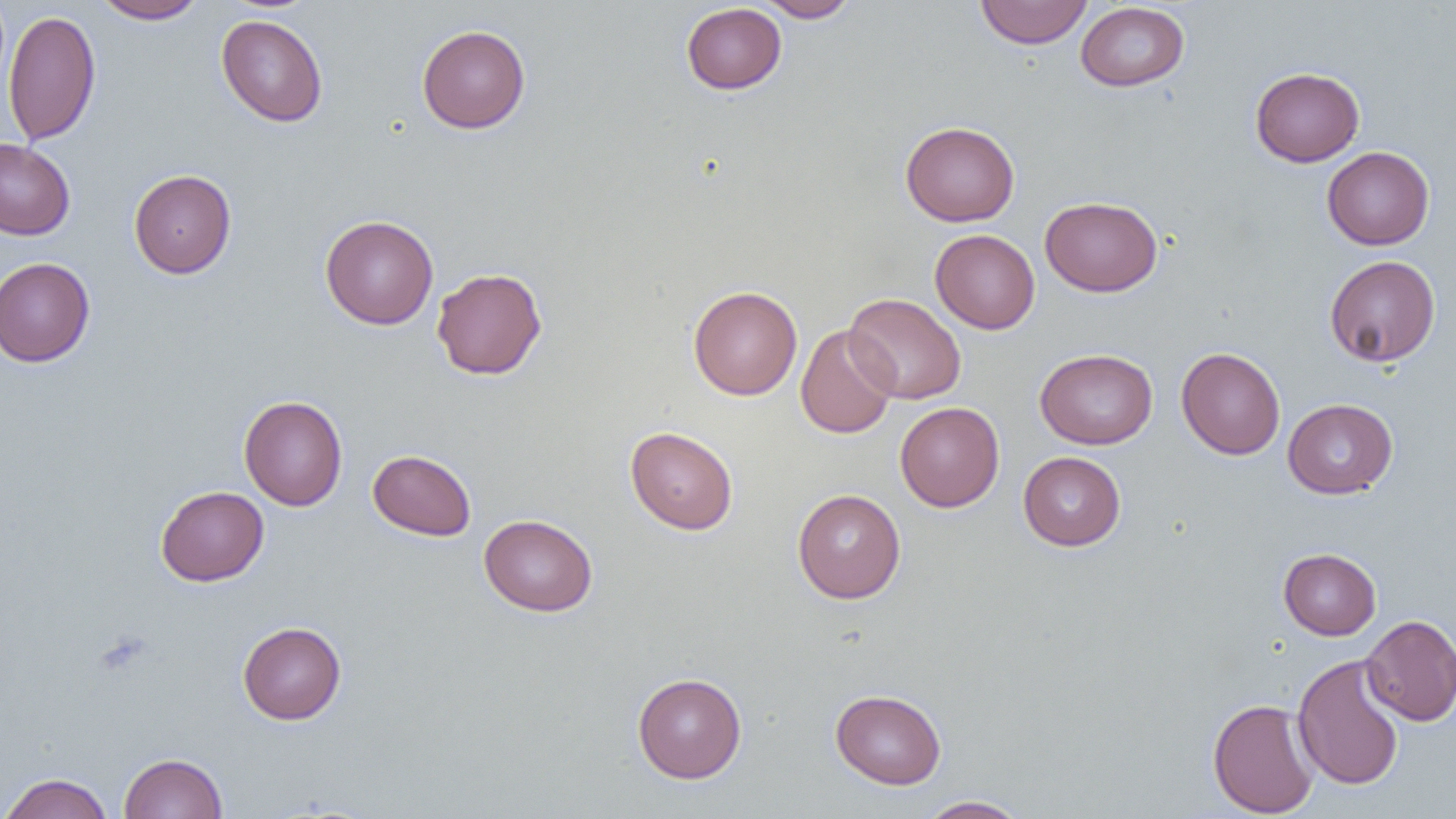

slide-level diagnosis = negative for blood parasites
modality = light microscopy
uninfected red blood cell locations = approximate bounding boxes as [x1, y1, x2, y2] in pixels: [92, 0, 209, 24], [755, 0, 860, 22], [975, 0, 1092, 48], [1075, 2, 1190, 92], [681, 3, 786, 95], [3, 8, 101, 146], [216, 14, 328, 127], [416, 24, 530, 133], [1250, 66, 1364, 167], [900, 121, 1020, 226], [0, 138, 75, 240], [1322, 146, 1434, 250], [128, 169, 236, 279], [1040, 195, 1162, 297], [320, 214, 438, 330], [930, 229, 1040, 334], [1324, 255, 1440, 367], [0, 257, 95, 367], [431, 267, 547, 380], [688, 285, 802, 400], [844, 293, 966, 405], [796, 324, 899, 439], [1176, 346, 1285, 460], [1034, 348, 1158, 449], [238, 395, 348, 511], [1282, 398, 1398, 499], [895, 402, 1004, 512], [625, 426, 738, 535], [368, 449, 477, 541], [1018, 451, 1126, 550], [155, 485, 269, 586], [792, 488, 906, 603], [479, 513, 598, 616], [1278, 548, 1381, 640], [1361, 614, 1456, 725], [237, 621, 346, 725], [1292, 653, 1405, 792], [632, 672, 747, 783], [830, 688, 946, 789], [1207, 697, 1320, 817], [119, 752, 227, 818], [0, 772, 114, 819], [916, 795, 1030, 818]
magnification = 1000x
preparation = thin blood film
field of view = single
image size = 1456×819 pixels